Report the malaria status of this cell.
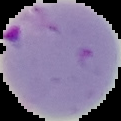

It is parasitized.

Summary:
  - Image type: segmented cell region on a black background
  - Preparation: thin blood smear
  - Image size: 121×121 pixels